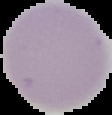 Result: no malaria parasites detected. From a thin blood film. Image is 112×115 pixels. Segmented cell region on a black background.